Assess this cell for malaria.
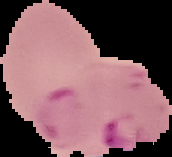

Parasitized.

Summary:
  - Image type: segmented cell region with the area outside set to black
  - Image size: 172×157 pixels
  - Preparation: thin blood smear